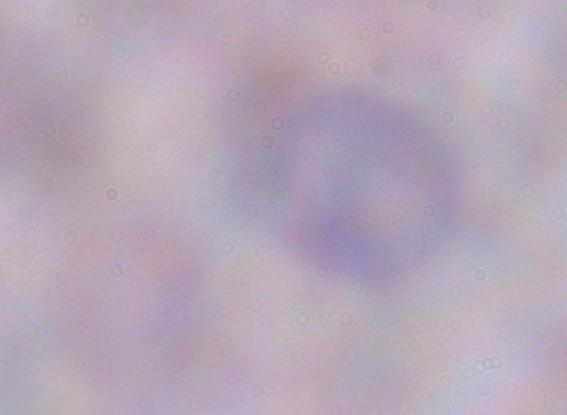 A trypanosome is shown. Captured at 1000x magnification. Micrograph.